Assess the morphology of the red blood cells.
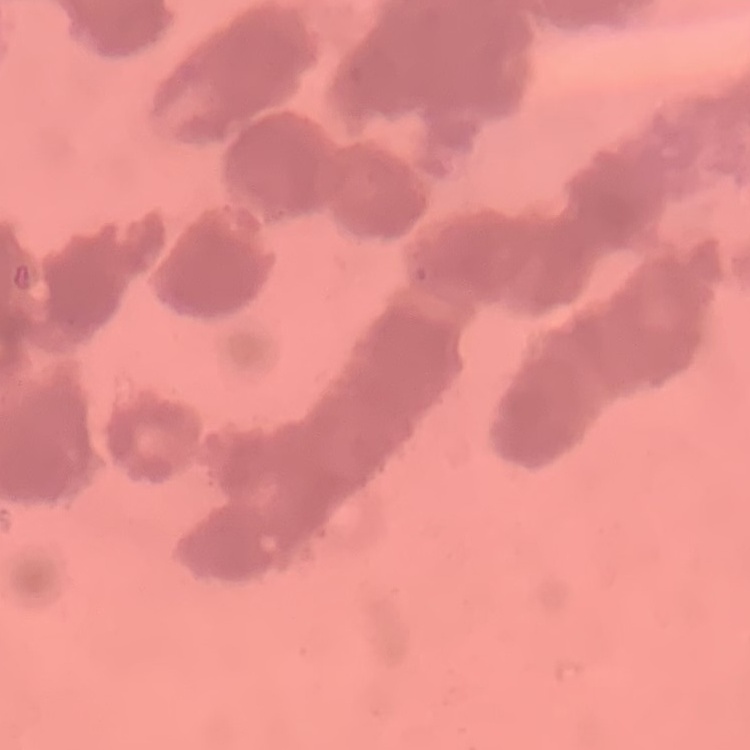

Rouleaux formation.

Summary:
  - Stain: Field's or Giemsa
  - Image type: square crop of a larger photomicrograph
  - Preparation: thin blood smear